Locate every uninfected red blood cell.
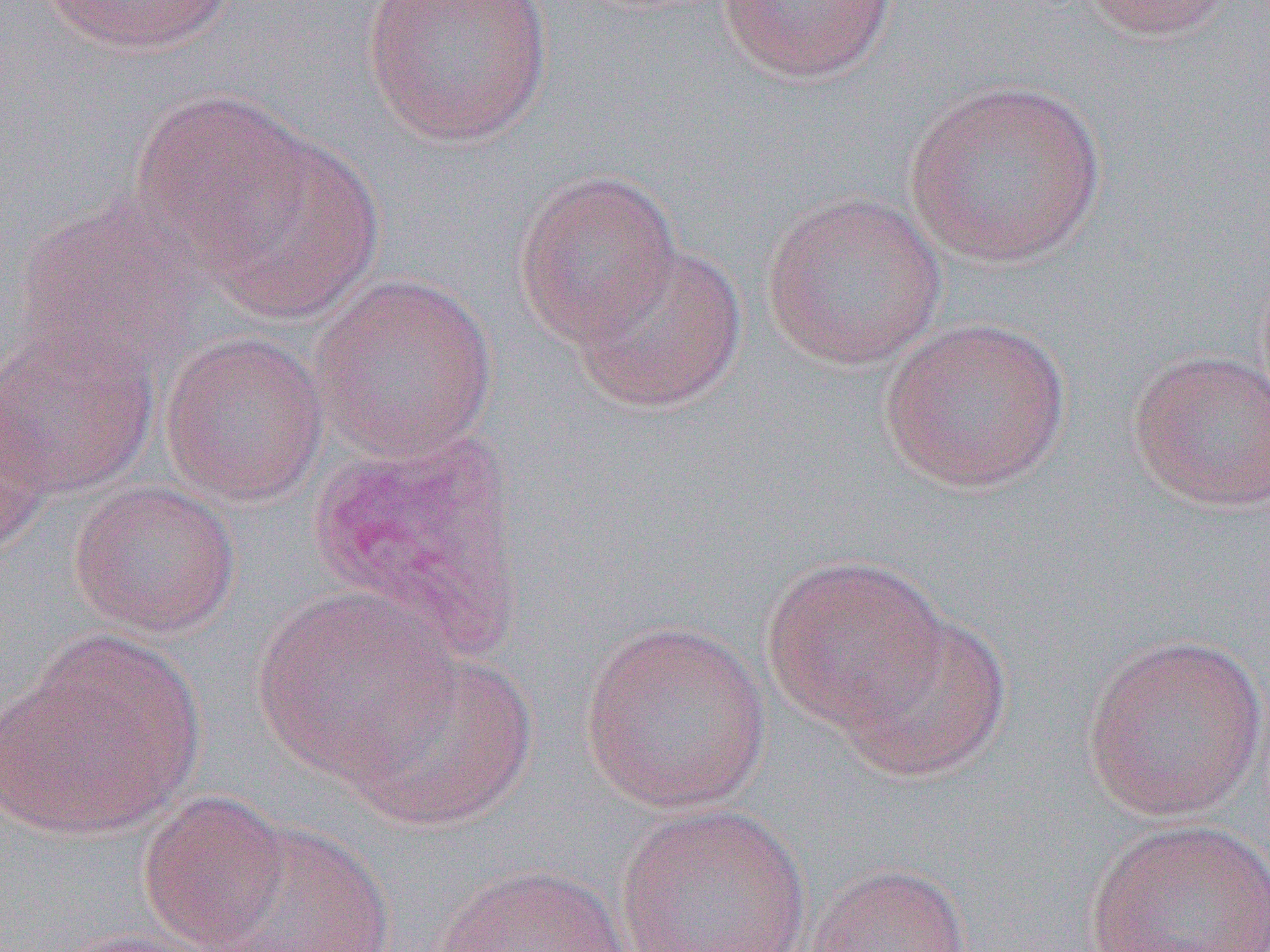

Approximate bounding boxes as [x1, y1, x2, y2] in pixels.
Uninfected red blood cells: [36, 0, 238, 55], [360, 0, 554, 148], [716, 0, 898, 84], [1080, 0, 1240, 41], [903, 78, 1107, 269], [129, 90, 315, 263], [196, 131, 384, 322], [512, 168, 683, 348], [760, 190, 947, 371], [13, 197, 205, 376], [569, 240, 749, 415], [308, 272, 498, 462], [878, 316, 1071, 495], [0, 321, 159, 498], [159, 330, 330, 507], [1128, 348, 1270, 514], [0, 400, 51, 558], [67, 480, 241, 638], [760, 553, 952, 734], [250, 587, 459, 782], [837, 609, 1013, 783], [579, 617, 771, 814], [2, 631, 205, 839], [1079, 633, 1268, 822], [342, 646, 538, 830], [136, 790, 294, 951], [614, 803, 813, 952], [1083, 818, 1270, 951], [202, 821, 395, 952], [805, 861, 972, 952], [432, 863, 634, 952], [43, 924, 233, 952].

Slide-level diagnosis: Plasmodium vivax. Image is 1270×952 pixels. Thin blood film. Single field of view. Light microscopy. 1000x magnification.